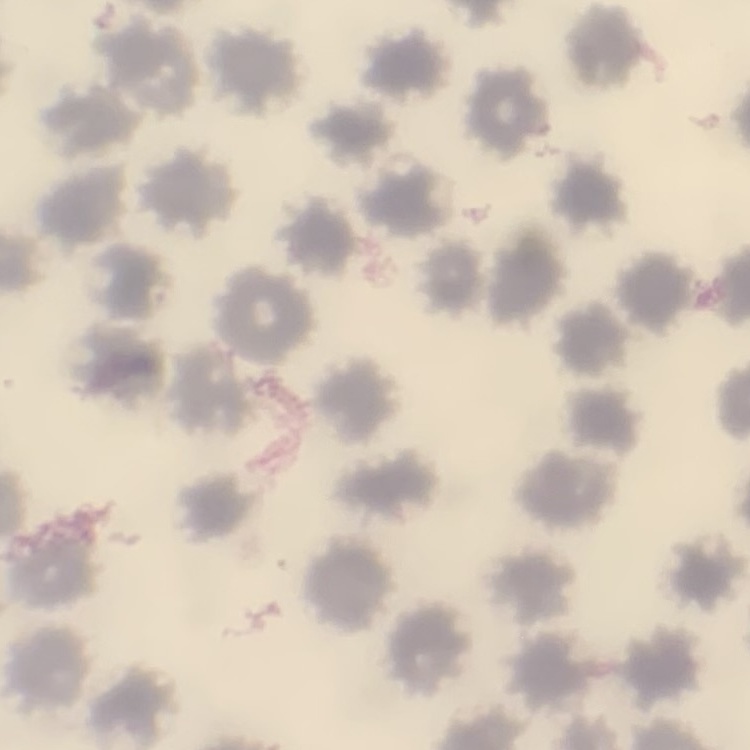 The erythrocytes exhibit no rouleaux formation. Field's or Giemsa stain. Thin blood film. One tile cut from a larger photomicrograph.